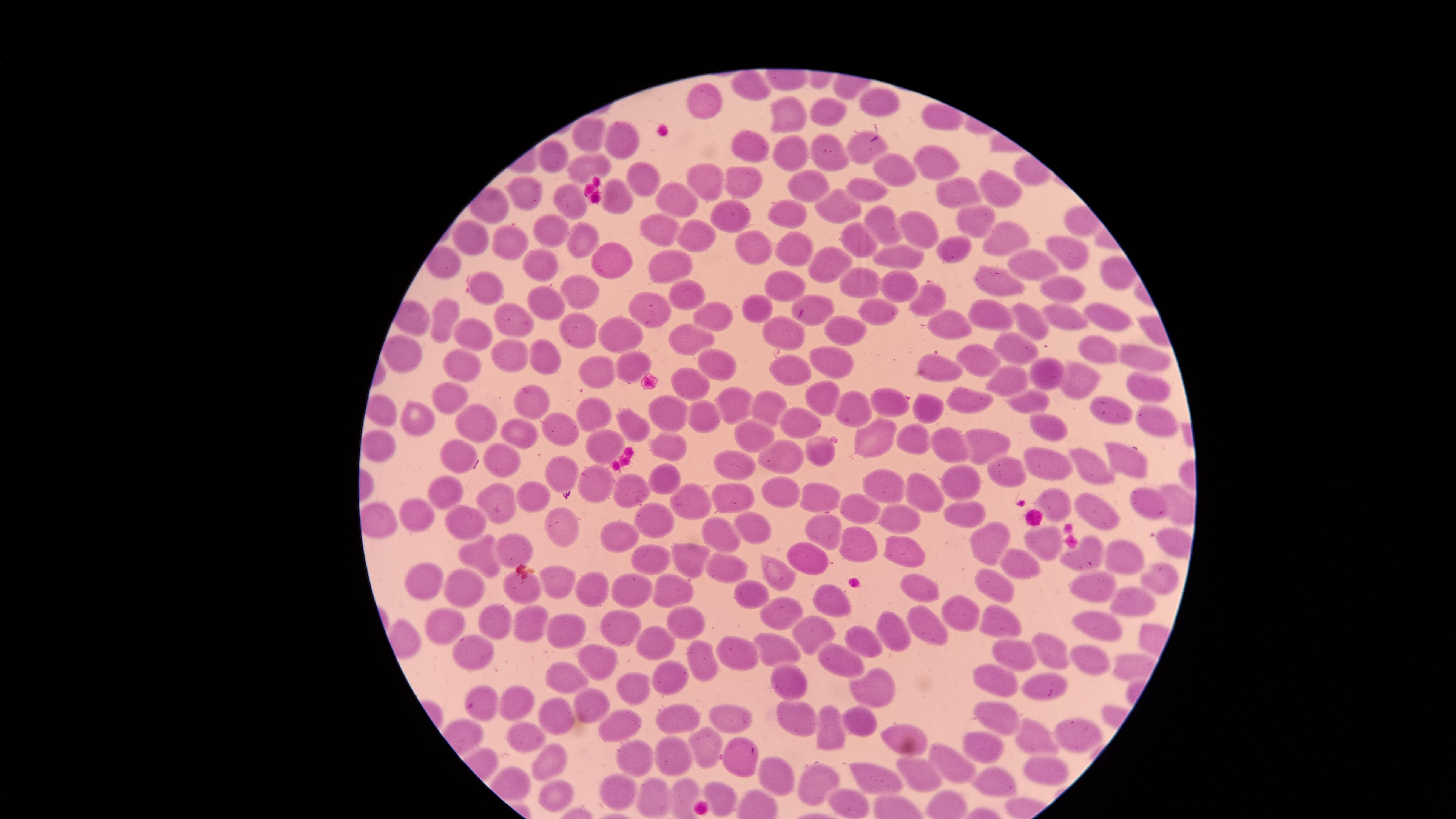

uninfected_red_blood_cells: 'approximate marker points as [x, y] in pixels: [746, 81], [879, 98], [709, 100], [824, 110], [786, 116], [592, 139], [620, 142], [752, 145], [864, 149], [835, 150], [788, 154], [550, 157], [940, 163], [586, 167], [893, 168], [735, 176], [647, 180], [703, 180], [809, 185], [868, 186], [1007, 188], [525, 191], [618, 196], [668, 196], [960, 196], [566, 201], [838, 206], [792, 215], [880, 219], [736, 220], [975, 222], [915, 224], [661, 228], [551, 230], [696, 233], [859, 235], [999, 239], [469, 240], [583, 240], [513, 243], [754, 249], [954, 250], [1061, 250], [799, 251], [903, 257], [615, 261], [1032, 261], [673, 263], [541, 266], [830, 268], [780, 278], [999, 281], [1060, 281], [864, 282], [486, 283], [900, 286], [582, 290], [683, 297], [930, 301], [815, 303], [546, 305], [650, 308], [759, 309], [881, 314], [716, 315], [991, 315], [512, 317], [1103, 317], [448, 319], [941, 319], [1028, 319], [1061, 319], [850, 327], [781, 331], [682, 333], [481, 334], [580, 334], [622, 335], [400, 349], [1015, 349], [1095, 349], [514, 356], [551, 357], [1141, 357], [978, 359], [466, 361], [837, 362], [636, 364], [937, 365], [713, 367], [792, 368], [596, 371], [1049, 372], [692, 379], [1075, 380], [1015, 381], [1151, 387], [450, 393], [826, 394], [1028, 394], [967, 398], [526, 401], [731, 401], [765, 404], [893, 404], [933, 407], [1110, 407], [851, 409], [671, 410], [587, 412], [705, 415], [478, 417], [422, 419], [796, 419], [1168, 421], [1046, 424], [558, 429], [633, 429], [523, 432], [751, 432], [866, 432], [987, 438], [914, 440], [667, 441], [958, 441], [379, 442], [817, 448], [607, 449], [783, 458], [507, 459], [1123, 459], [463, 460], [735, 461], [1049, 461], [564, 469], [1097, 469], [1010, 473], [652, 478], [884, 480], [597, 481], [963, 484], [449, 488], [630, 489], [533, 491], [736, 493], [782, 494], [821, 495], [919, 495], [1055, 499], [496, 501], [693, 501], [1149, 502], [960, 511], [860, 513], [905, 513], [416, 516], [1100, 516], [462, 522], [655, 523], [559, 524], [750, 524], [825, 526], [715, 534], [985, 538], [1043, 539], [620, 541], [854, 544], [516, 548], [1084, 548], [902, 549], [486, 551], [1130, 553], [692, 555], [652, 558], [807, 558], [718, 564], [1023, 565], [778, 575], [427, 576], [1158, 576], [558, 582], [994, 583], [674, 585], [459, 586], [593, 586], [630, 586], [916, 587], [525, 589], [1094, 589], [753, 594], [828, 600], [1140, 600], [775, 612], [967, 614], [1000, 617], [491, 618], [525, 619], [1094, 622], [930, 623], [454, 628], [618, 628], [689, 628], [813, 630], [897, 630], [559, 633], [862, 637], [655, 644], [779, 646], [1058, 649], [734, 652], [1016, 652], [475, 653], [838, 657], [1088, 658], [700, 661], [593, 664], [566, 675], [668, 676], [992, 678], [789, 681], [634, 686], [1052, 687], [877, 690], [514, 701], [586, 704], [481, 711], [797, 711], [733, 714], [1000, 716], [680, 718], [548, 719], [828, 722], [857, 722], [619, 724], [896, 728], [527, 733], [1073, 734], [1033, 738], [982, 744], [702, 745], [674, 751], [544, 757], [636, 757], [950, 759], [743, 760], [1039, 768], [772, 775], [918, 776], [875, 777], [820, 782], [995, 783], [620, 787], [557, 792], [716, 794], [651, 796], [851, 802]'
image_size: 1456×819 pixels
presence: no malaria parasites detected
visible_region: circular
field_of_view: single
stain: Giemsa
preparation: thin blood smear
capture: smartphone photograph through the microscope eyepiece